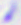
Photomicrograph. 400x magnification. Toxoplasma gondii is shown.